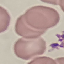

Summary:
  - Result: no malaria parasites detected
  - Image type: automatically extracted cell patch, resized to 64 × 64 pixels
  - Stain: Giemsa
  - Preparation: thin smear
  - Capture: smartphone camera at the microscope eyepiece